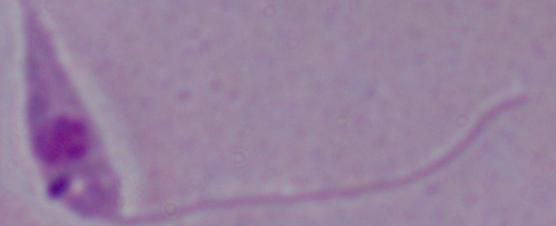

magnification = 1000x
identification = Leishmania
modality = micrograph